Classify this cell by malaria status.
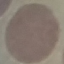
It is uninfected.

Cell patch, automatically extracted from a larger field of view and resized to 64 × 64 pixels. Thin blood smear. Photographed with a smartphone camera at the microscope eyepiece. Giemsa stain.